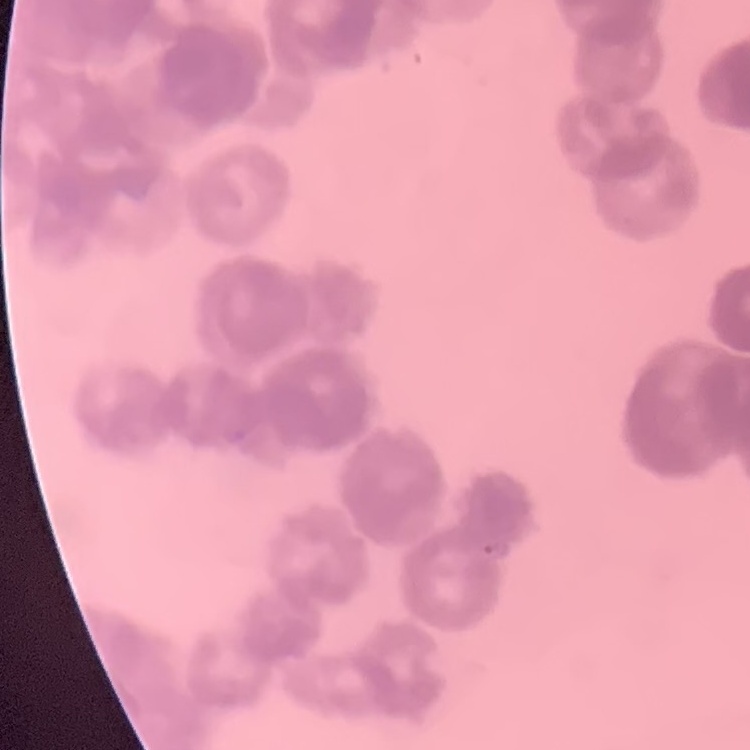
Summary:
  - Erythrocyte morphology: rouleaux formation
  - Stain: Field's or Giemsa
  - Image type: square crop of a larger photomicrograph
  - Preparation: thin peripheral smear